Comment on the morphology of the erythrocytes.
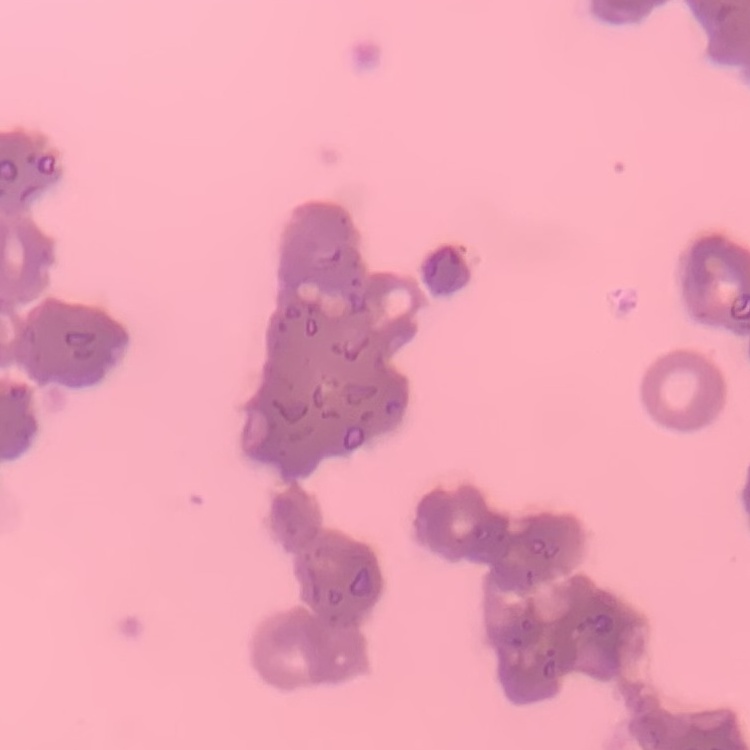

Rouleaux formation.

Field's or Giemsa stain. One tile cut from a larger photomicrograph. Thin blood film.